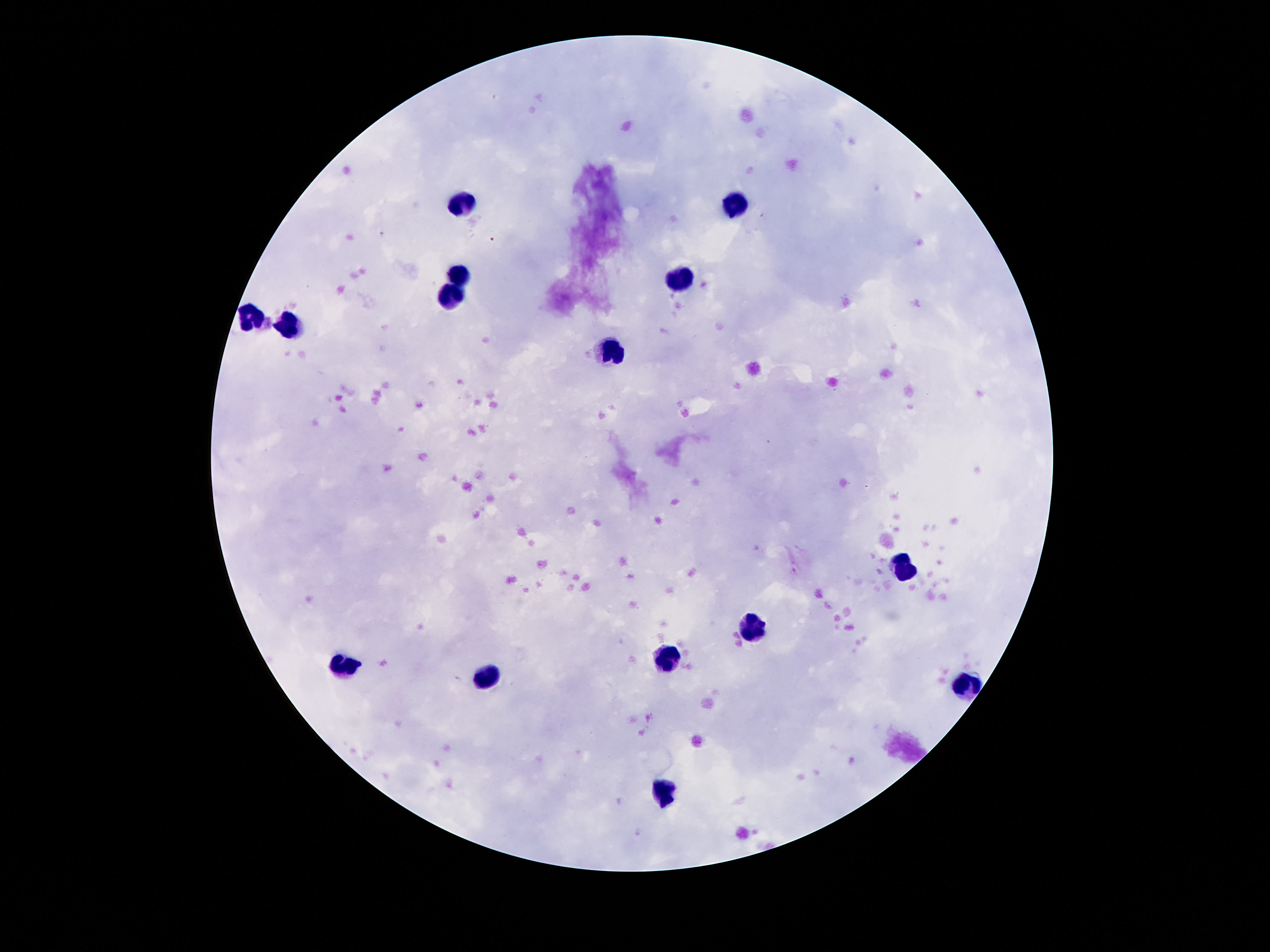
Approximate centers as {x, y} in pixels.
Summary:
  - Leukocyte locations: {463, 200}, {741, 204}, {459, 275}, {678, 280}, {452, 299}, {254, 317}, {291, 325}, {610, 351}, {902, 568}, {754, 630}, {665, 658}, {347, 665}, {493, 672}, {973, 688}, {666, 794}
  - Field of view: one from this slide
  - Capture: smartphone camera through the microscope eyepiece
  - Stain: Giemsa
  - Preparation: thick blood smear
  - Image size: 1270×952 pixels
  - Magnification: 100x
  - Patient malaria status: not infected